Locate every malaria parasite.
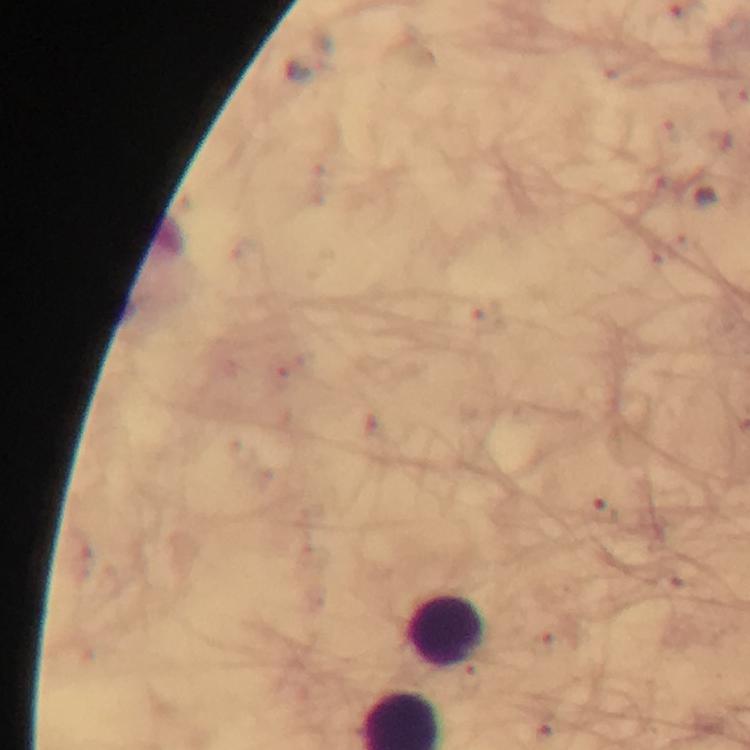

No malaria parasites detected.

{
  "context": "from a malaria diagnostic workup",
  "stain": "Giemsa",
  "cropped_from": "one field of view",
  "image_size": "750×750 pixels",
  "magnification": "100x",
  "preparation": "thick blood smear",
  "leukocyte_locations": "approximate centers as [x, y] in pixels: [446, 634]",
  "immersion_oil": "applied",
  "capture": "smartphone mounted on the microscope"
}